Comment on the morphology of the red blood cells.
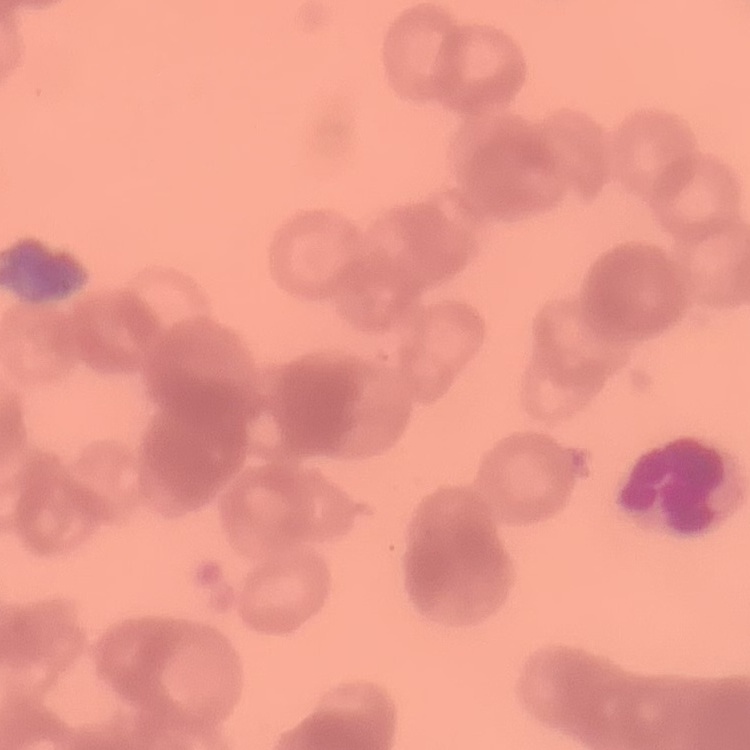

Rouleaux formation.

preparation: thin peripheral smear
image_type: one tile cut from a larger photomicrograph
stain: Field's or Giemsa